Point out each malaria parasite.
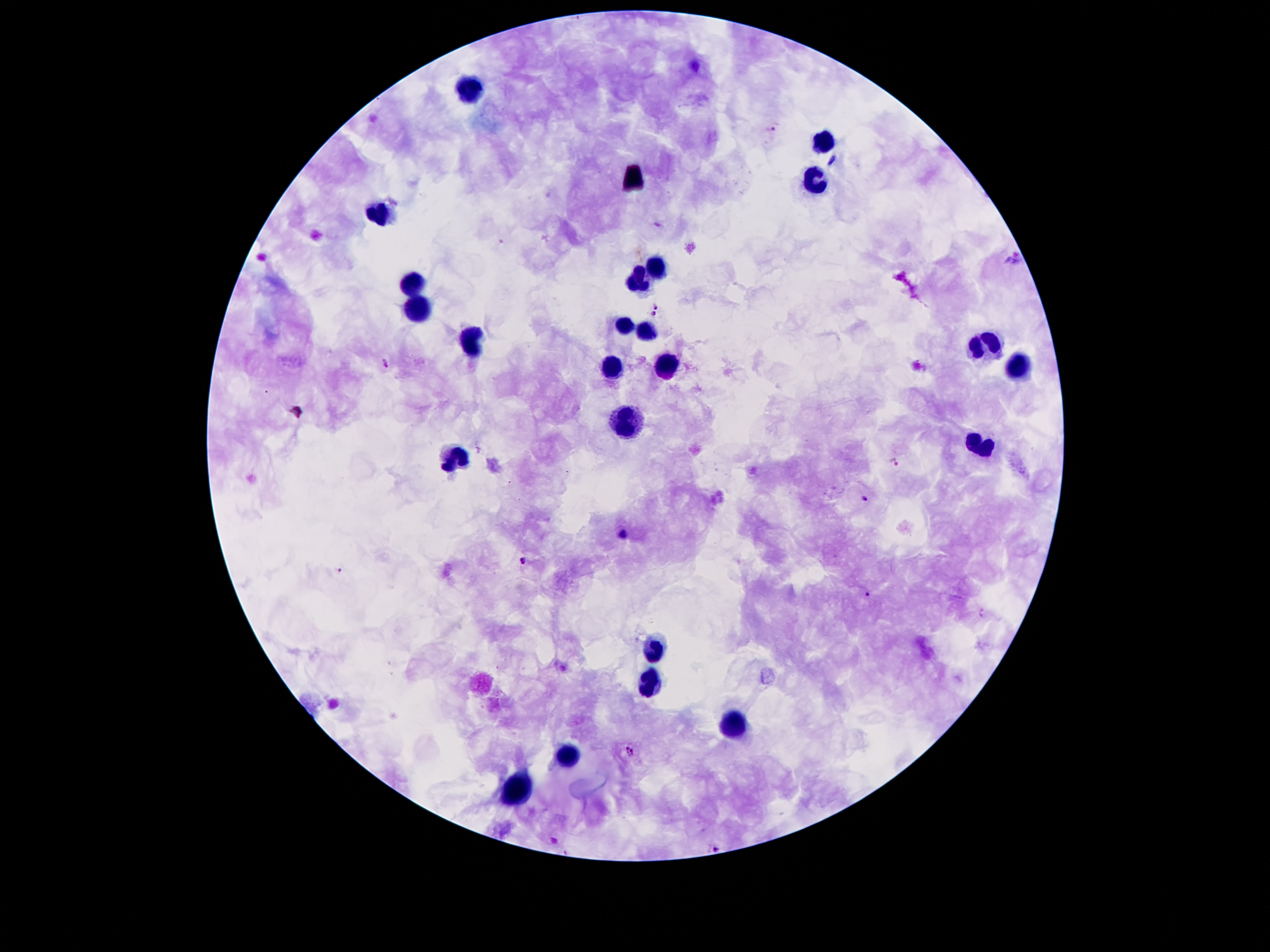
Approximate centers as (x, y) in pixels.
Malaria parasites: (771, 129), (833, 161), (655, 306), (654, 314), (385, 362), (894, 462), (863, 498), (621, 534), (523, 561), (340, 569), (869, 594), (630, 750), (717, 847).

Summary:
  - Leukocyte locations: (472, 88), (820, 141), (815, 182), (383, 213), (659, 270), (639, 280), (414, 285), (421, 309), (627, 325), (645, 331), (987, 343), (472, 345), (666, 366), (1019, 367), (616, 373), (627, 421), (975, 446), (457, 458), (656, 649), (651, 682), (735, 726), (572, 753), (519, 791)
  - Stain: Giemsa
  - Patient malaria status: positive for Plasmodium falciparum
  - Field of view: one from this slide
  - Image size: 1270×952 pixels
  - Magnification: 100x
  - Capture: smartphone camera through the microscope eyepiece
  - Preparation: thick blood film